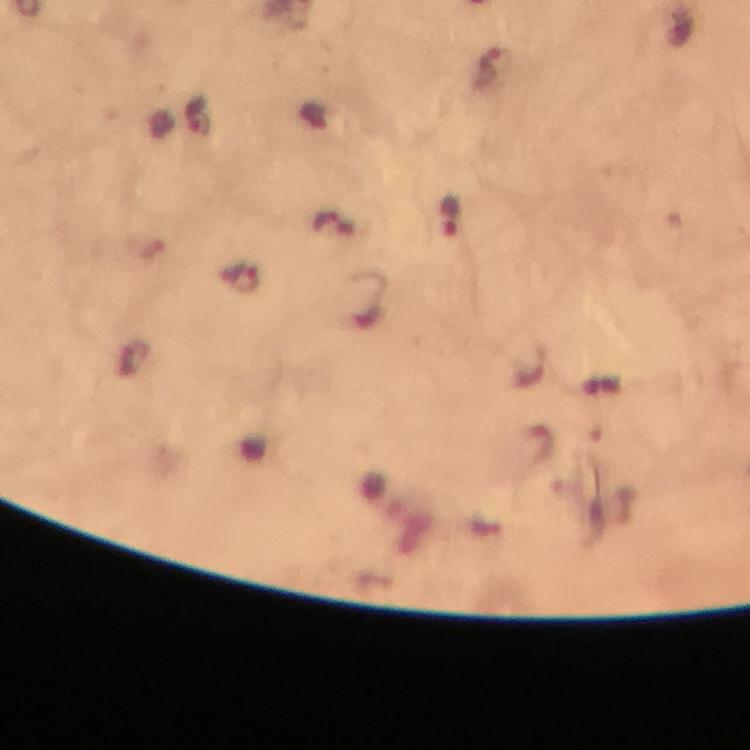 Approximate centers as {x, y} in pixels. Plasmodium parasite locations: {491, 70}, {197, 114}, {451, 217}, {241, 279}. Immersion oil was used. Photographed with a smartphone mounted on the microscope. Giemsa stain. 100x magnification. Image is 750×750 pixels. Thick blood film. Cropped region of a single field of view. From a diagnostic examination for malaria.